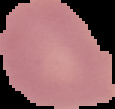
Malaria status: uninfected. From a thin blood smear. Cell region segmented out of the field of view; the surrounding area is masked to black. Image is 115×109 pixels.